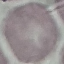
Summary:
  - Malaria status: uninfected
  - Image type: automatically extracted cell patch, resized to 64 × 64 pixels
  - Capture: smartphone camera at the microscope eyepiece
  - Preparation: thin blood smear
  - Stain: Giemsa